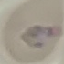

Summary:
  - Malaria status: parasitized
  - Image type: cell patch, automatically extracted from a larger field of view and resized to 64 × 64 pixels
  - Stain: Giemsa
  - Preparation: thin blood smear
  - Capture: smartphone through the microscope eyepiece